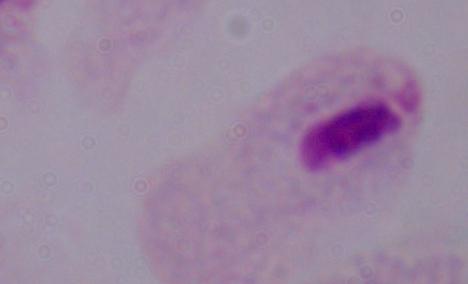
magnification: 1000x
identification: trichomonad
modality: photomicrograph